Describe the morphology of the erythrocytes.
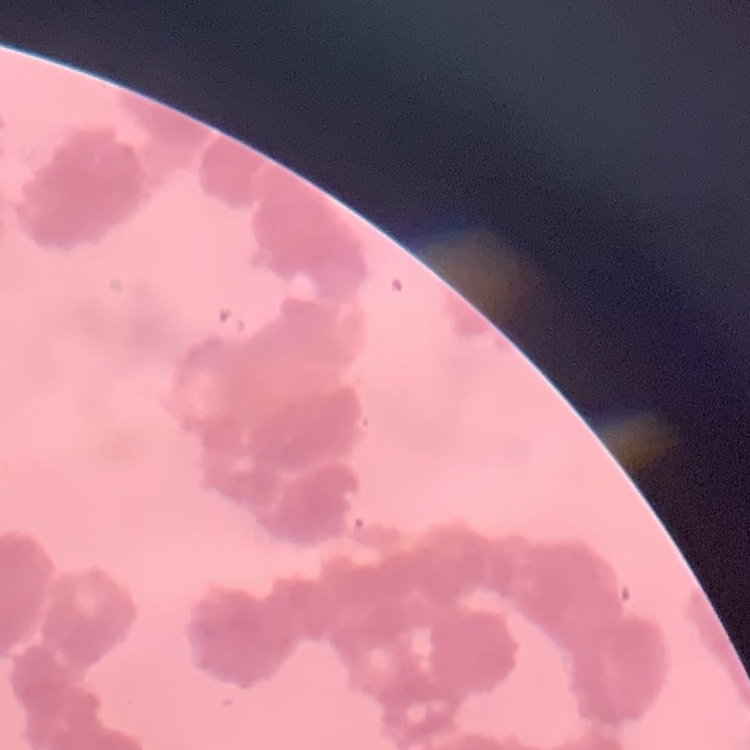

They show rouleaux formation.

image type = square crop of a larger photomicrograph
stain = Field's or Giemsa
preparation = thin peripheral smear